Identify the blood parasite species.
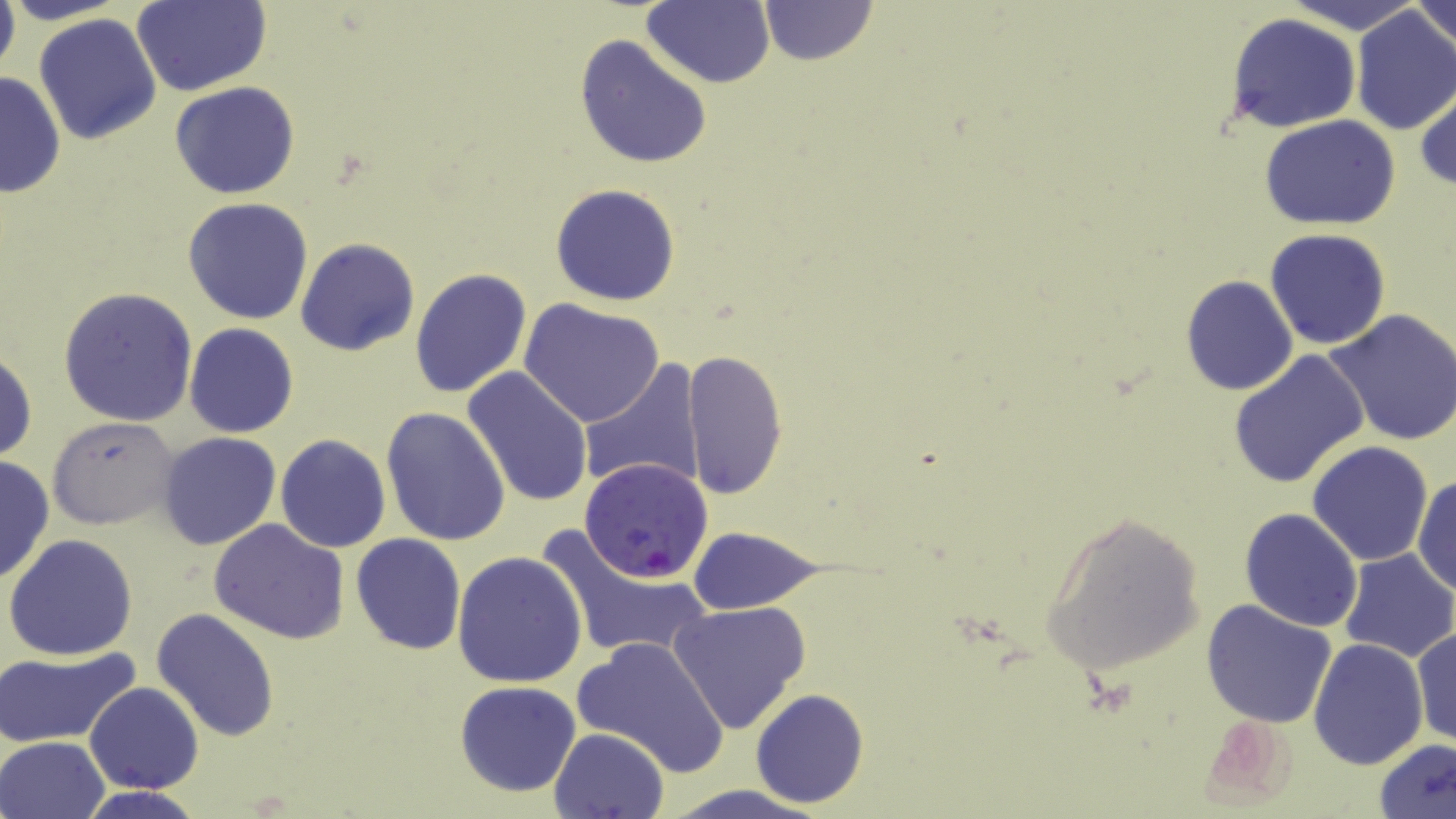

Plasmodium falciparum.

{
  "modality": "optical microscopy",
  "preparation": "thin blood film",
  "plasmodium_falciparum_infected_red_blood_cell_locations": "approximate bounding boxes as (x1, y1, x2, y2) in pixels: (580, 456, 713, 581)",
  "image_size": "1456×819 pixels",
  "stain": "May-Grünwald-Giemsa",
  "uninfected_red_blood_cell_locations": "approximate bounding boxes as (x1, y1, x2, y2) in pixels: (3, 0, 130, 26), (758, 0, 879, 66), (1286, 0, 1426, 32), (1411, 0, 1456, 50), (0, 1, 21, 83), (133, 1, 270, 96), (642, 2, 775, 88), (1349, 5, 1456, 136), (34, 13, 162, 145), (1227, 13, 1363, 133), (574, 37, 712, 169), (0, 70, 66, 198), (1415, 81, 1456, 193), (170, 82, 300, 200), (1260, 114, 1402, 231), (549, 183, 680, 307), (183, 197, 313, 323), (1264, 228, 1392, 350), (295, 237, 419, 356), (408, 266, 531, 399), (1179, 274, 1298, 397), (59, 287, 198, 426), (520, 299, 664, 429), (1325, 308, 1456, 448), (184, 323, 299, 438), (0, 345, 37, 464), (1226, 347, 1371, 489), (684, 348, 789, 500), (581, 361, 706, 493), (463, 366, 593, 508), (381, 406, 511, 546), (48, 416, 180, 531), (155, 432, 282, 551), (275, 434, 391, 552), (1306, 441, 1434, 567), (0, 453, 54, 586), (1412, 474, 1456, 596), (1239, 508, 1363, 631), (1038, 510, 1206, 676), (208, 519, 351, 643), (535, 523, 711, 664), (686, 525, 823, 614), (350, 533, 467, 656), (5, 534, 139, 661), (1338, 549, 1455, 662), (452, 550, 587, 688), (1200, 598, 1338, 728), (667, 602, 812, 735), (151, 608, 278, 740), (1409, 625, 1455, 749), (571, 636, 732, 774), (1308, 638, 1428, 769), (2, 647, 139, 747), (455, 681, 582, 798), (84, 683, 204, 794), (750, 688, 869, 807), (1195, 709, 1302, 811), (549, 726, 669, 818), (1, 735, 109, 819), (1372, 737, 1456, 819), (656, 785, 832, 819), (75, 786, 204, 818)",
  "magnification": "1000x",
  "field_of_view": "one of a larger specimen"
}